State the blood parasite species.
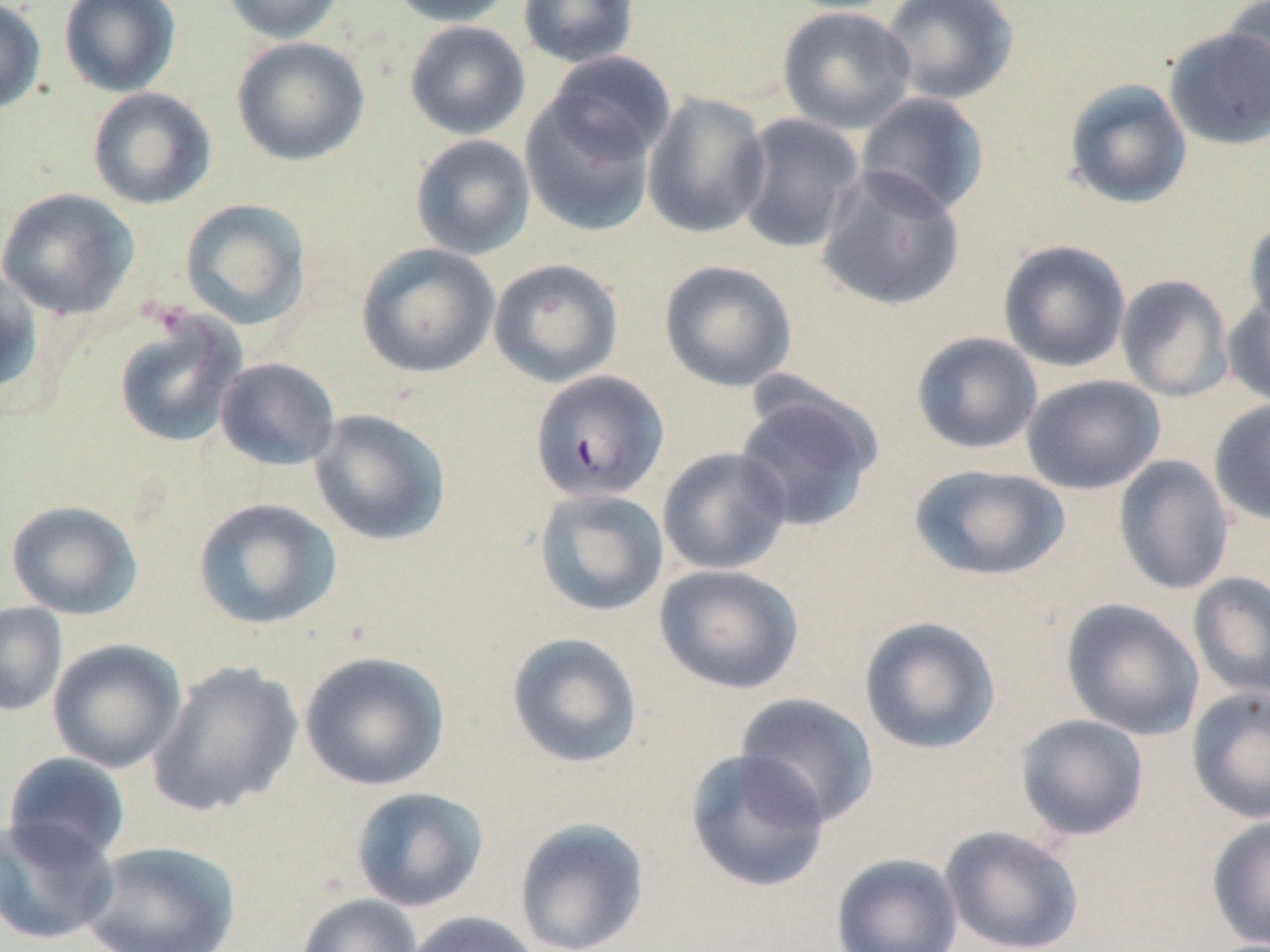
Plasmodium falciparum.

magnification = 1000x
stain = May-Grünwald-Giemsa
Plasmodium falciparum-infected red blood cell locations = approximate bounding boxes as named x1/y1/x2/y2 corners in pixels: (x1=530, y1=369, x2=669, y2=503)
preparation = thin blood film
image size = 1270×952 pixels
field of view = one of a larger specimen
uninfected red blood cell locations = approximate bounding boxes as named x1/y1/x2/y2 corners in pixels: (x1=0, y1=0, x2=47, y2=114), (x1=58, y1=0, x2=181, y2=97), (x1=220, y1=0, x2=347, y2=44), (x1=385, y1=0, x2=515, y2=27), (x1=517, y1=0, x2=639, y2=68), (x1=880, y1=0, x2=1019, y2=106), (x1=1221, y1=0, x2=1269, y2=121), (x1=777, y1=6, x2=916, y2=134), (x1=404, y1=21, x2=530, y2=140), (x1=1163, y1=27, x2=1270, y2=150), (x1=231, y1=37, x2=370, y2=166), (x1=545, y1=51, x2=676, y2=164), (x1=1064, y1=79, x2=1193, y2=209), (x1=87, y1=87, x2=217, y2=210), (x1=519, y1=88, x2=659, y2=237), (x1=642, y1=91, x2=771, y2=239), (x1=856, y1=92, x2=990, y2=218), (x1=734, y1=112, x2=866, y2=254), (x1=410, y1=134, x2=536, y2=259), (x1=816, y1=164, x2=966, y2=311), (x1=0, y1=187, x2=140, y2=320), (x1=179, y1=198, x2=311, y2=330), (x1=1242, y1=215, x2=1270, y2=335), (x1=997, y1=239, x2=1131, y2=373), (x1=355, y1=243, x2=500, y2=379), (x1=488, y1=258, x2=624, y2=388), (x1=658, y1=260, x2=798, y2=392), (x1=0, y1=269, x2=44, y2=395), (x1=1115, y1=274, x2=1234, y2=402), (x1=1223, y1=294, x2=1270, y2=408), (x1=113, y1=313, x2=248, y2=448), (x1=911, y1=332, x2=1043, y2=455), (x1=215, y1=357, x2=341, y2=471), (x1=1021, y1=374, x2=1165, y2=495), (x1=733, y1=384, x2=882, y2=533), (x1=1209, y1=399, x2=1270, y2=527), (x1=309, y1=409, x2=451, y2=547), (x1=657, y1=446, x2=792, y2=575), (x1=1113, y1=455, x2=1234, y2=596), (x1=908, y1=464, x2=1071, y2=582), (x1=533, y1=488, x2=669, y2=616), (x1=192, y1=497, x2=342, y2=630), (x1=5, y1=500, x2=143, y2=620), (x1=654, y1=563, x2=804, y2=695), (x1=1188, y1=572, x2=1270, y2=700), (x1=1061, y1=598, x2=1205, y2=740), (x1=0, y1=602, x2=68, y2=717), (x1=858, y1=616, x2=1001, y2=755), (x1=507, y1=632, x2=643, y2=768), (x1=47, y1=639, x2=187, y2=773), (x1=299, y1=651, x2=450, y2=791), (x1=147, y1=660, x2=302, y2=817), (x1=1186, y1=686, x2=1270, y2=824), (x1=734, y1=693, x2=881, y2=828), (x1=1015, y1=714, x2=1150, y2=841), (x1=685, y1=748, x2=831, y2=893), (x1=2, y1=752, x2=132, y2=866), (x1=350, y1=787, x2=489, y2=912), (x1=1206, y1=814, x2=1270, y2=950), (x1=0, y1=815, x2=120, y2=946), (x1=513, y1=817, x2=650, y2=952), (x1=939, y1=824, x2=1085, y2=952), (x1=79, y1=840, x2=242, y2=951), (x1=831, y1=851, x2=964, y2=952), (x1=296, y1=893, x2=423, y2=952), (x1=401, y1=910, x2=544, y2=952)
platelet locations = approximate bounding boxes as named x1/y1/x2/y2 corners in pixels: (x1=141, y1=297, x2=195, y2=337)
modality = light microscopy